Assess the morphology of the red blood cells.
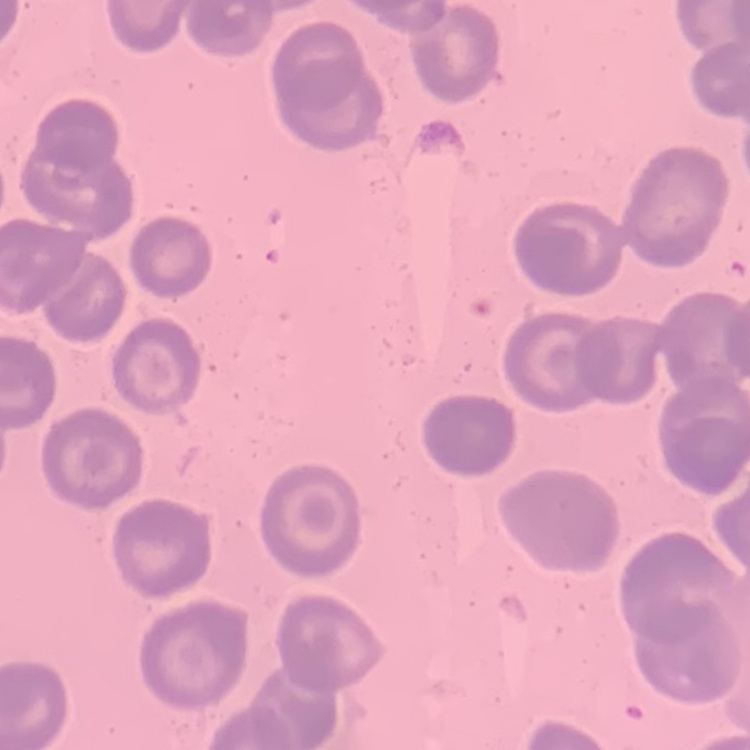

They show no rouleaux formation.

Field's or Giemsa stain. Thin peripheral smear. Square crop of a larger photomicrograph.